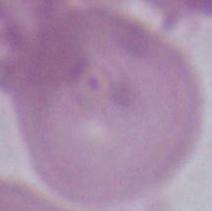
Captured at 1000x magnification. Photomicrograph. An erythrocyte is shown.